Classify this cell by malaria status.
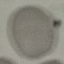
It is uninfected.

Automatically extracted cell patch, resized to 64 × 64 pixels. Acquired by smartphone through the microscope eyepiece. Thin blood smear. Giemsa-stained preparation.